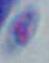

identification: Toxoplasma gondii
modality: micrograph
magnification: 1000x